Classify this cell by malaria status.
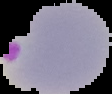
Parasitized.

image size = 112×94 pixels
image type = segmented cell region with the area outside set to black
preparation = thin blood film